Report the malaria status of this cell.
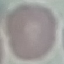

It is uninfected.

Summary:
  - Preparation: thin blood film
  - Image type: cell patch, automatically extracted from a larger field of view and resized to 64 × 64 pixels
  - Capture: smartphone camera at the microscope eyepiece
  - Stain: Giemsa